Classify this cell by malaria status.
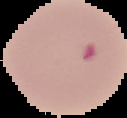
It is uninfected.

From a thin blood smear. Segmented cell region on a black background. Image is 127×118 pixels.